Classify this cell by malaria status.
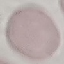

It is uninfected.

Acquired by smartphone through the microscope eyepiece. Cell patch, automatically extracted from a larger field of view and resized to 64 × 64 pixels. Thin smear of blood. Giemsa-stained preparation.